Classify this cell by malaria status.
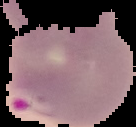

It is parasitized.

Summary:
  - Preparation: thin blood film
  - Image type: segmented cell region with the area outside set to black
  - Image size: 136×127 pixels